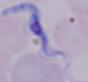
Summary:
  - Magnification: 1000x
  - Identification: trypanosome
  - Modality: micrograph